State which parasite is depicted.
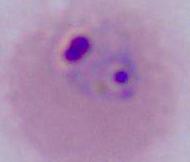
This is Plasmodium.

Summary:
  - Modality: micrograph
  - Magnification: 400x or 1000x